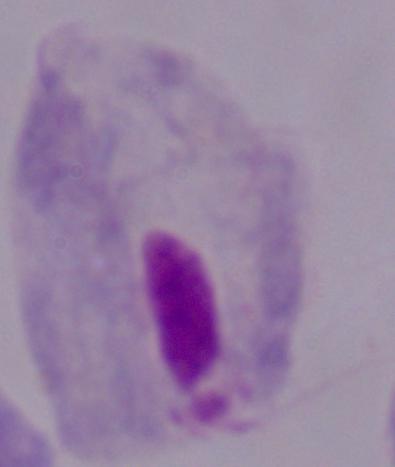
Summary:
  - Identification: trichomonad
  - Modality: photomicrograph
  - Magnification: 1000x